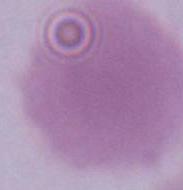
1000x magnification. Photomicrograph. A red blood cell is shown.